Describe the morphology of the red blood cells.
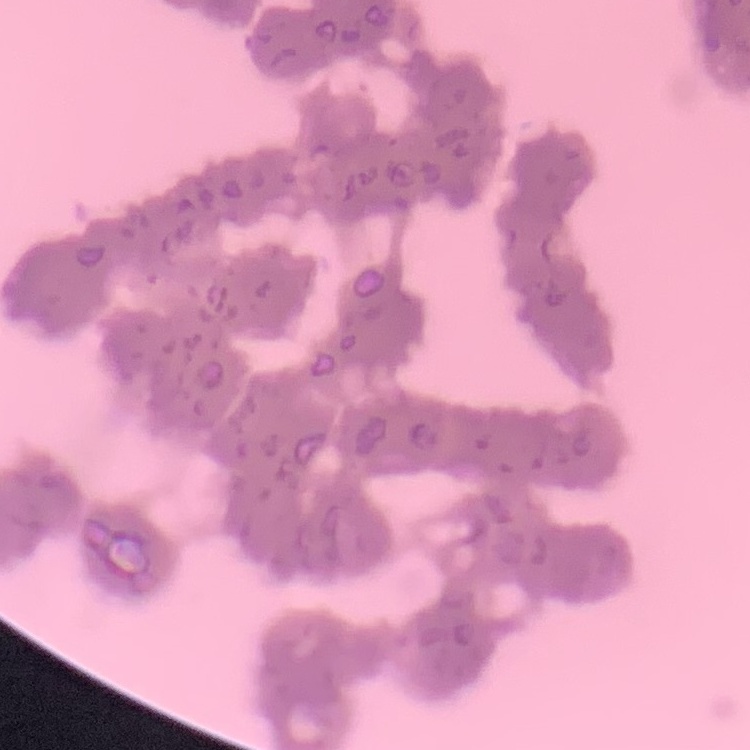

They show rouleaux formation.

Summary:
  - Image type: square crop of a larger photomicrograph
  - Stain: Field's or Giemsa
  - Preparation: thin blood film